Identify the parasite.
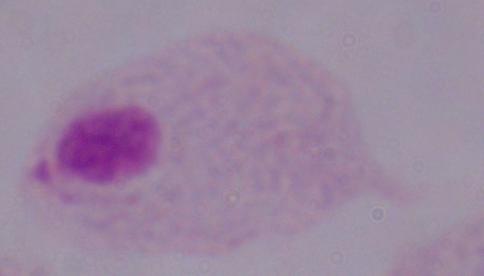
This is a trichomonad.

modality = photomicrograph
magnification = 1000x